Assess this cell for malaria.
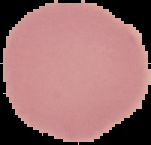

Uninfected.

Summary:
  - Preparation: thin blood smear
  - Image size: 151×145 pixels
  - Image type: segmented cell region with the area outside set to black